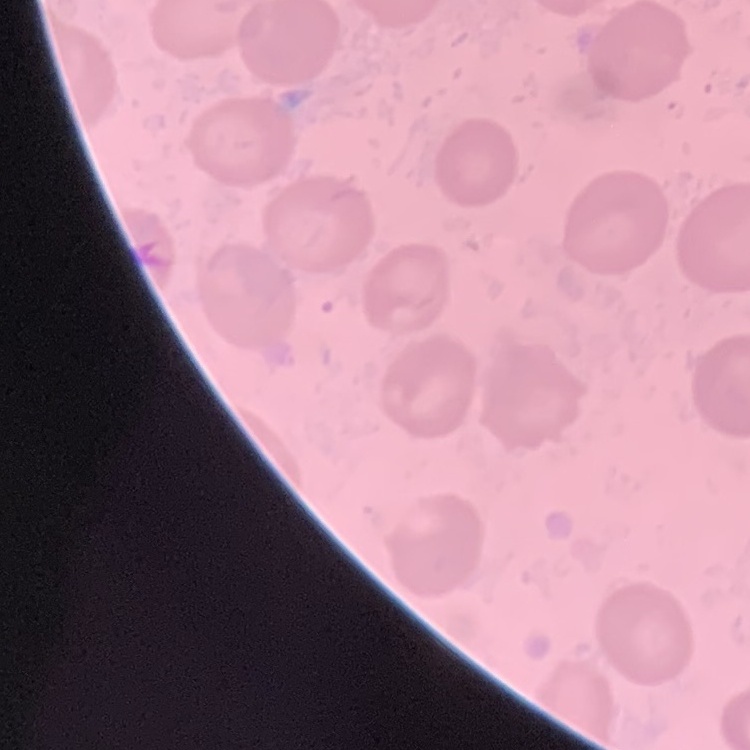 The red blood cells exhibit no rouleaux formation. One tile cut from a larger photomicrograph. Field's or Giemsa stain. Thin blood film.